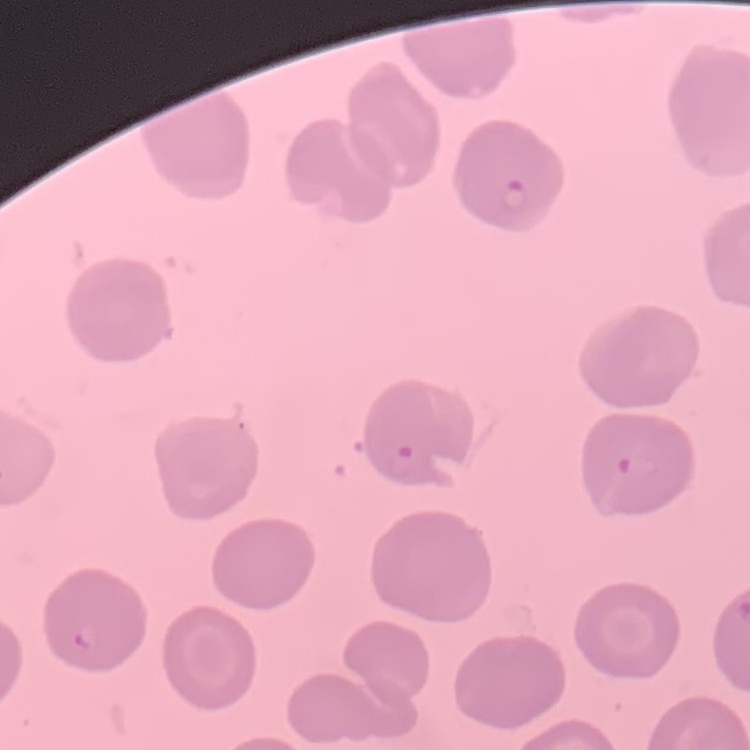
Summary:
  - Red blood cell morphology: no rouleaux formation
  - Preparation: thin blood film
  - Stain: Field's or Giemsa
  - Image type: square crop of a larger photomicrograph